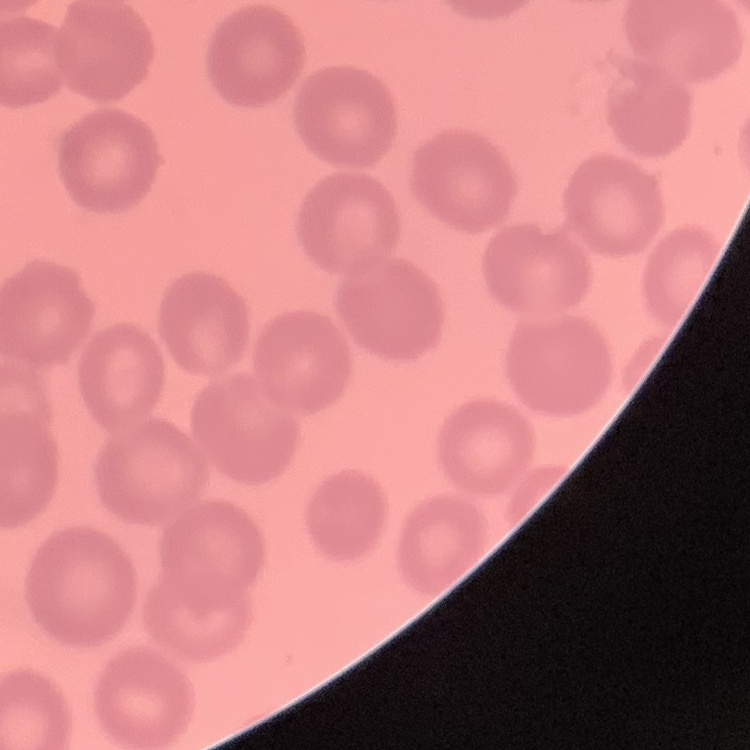

The red blood cells exhibit no rouleaux formation. One tile cut from a larger photomicrograph. Stained with either Field's or Giemsa. Thin peripheral smear.